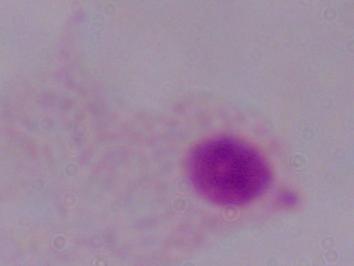

Summary:
  - Identification: trichomonad
  - Magnification: 1000x
  - Modality: micrograph